Report the malaria status of this cell.
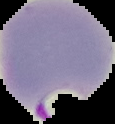

It is parasitized.

{
  "image_size": "115×124 pixels",
  "preparation": "thin blood smear",
  "image_type": "segmented cell region on a black background"
}